Assess this cell for malaria.
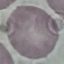
Uninfected.

{
  "stain": "Giemsa",
  "preparation": "thin blood film",
  "capture": "smartphone camera at the microscope eyepiece",
  "image_type": "automatically extracted cell patch, resized to 64 × 64 pixels"
}